Describe the morphology of the red blood cells.
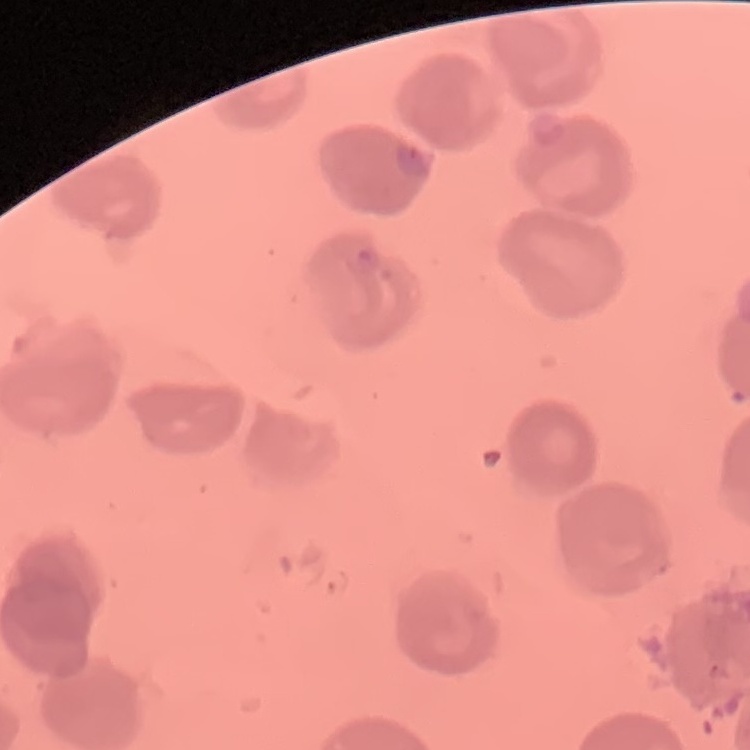
They show no rouleaux formation.

Thin blood smear. One tile cut from a larger photomicrograph. Stained with either Field's or Giemsa.